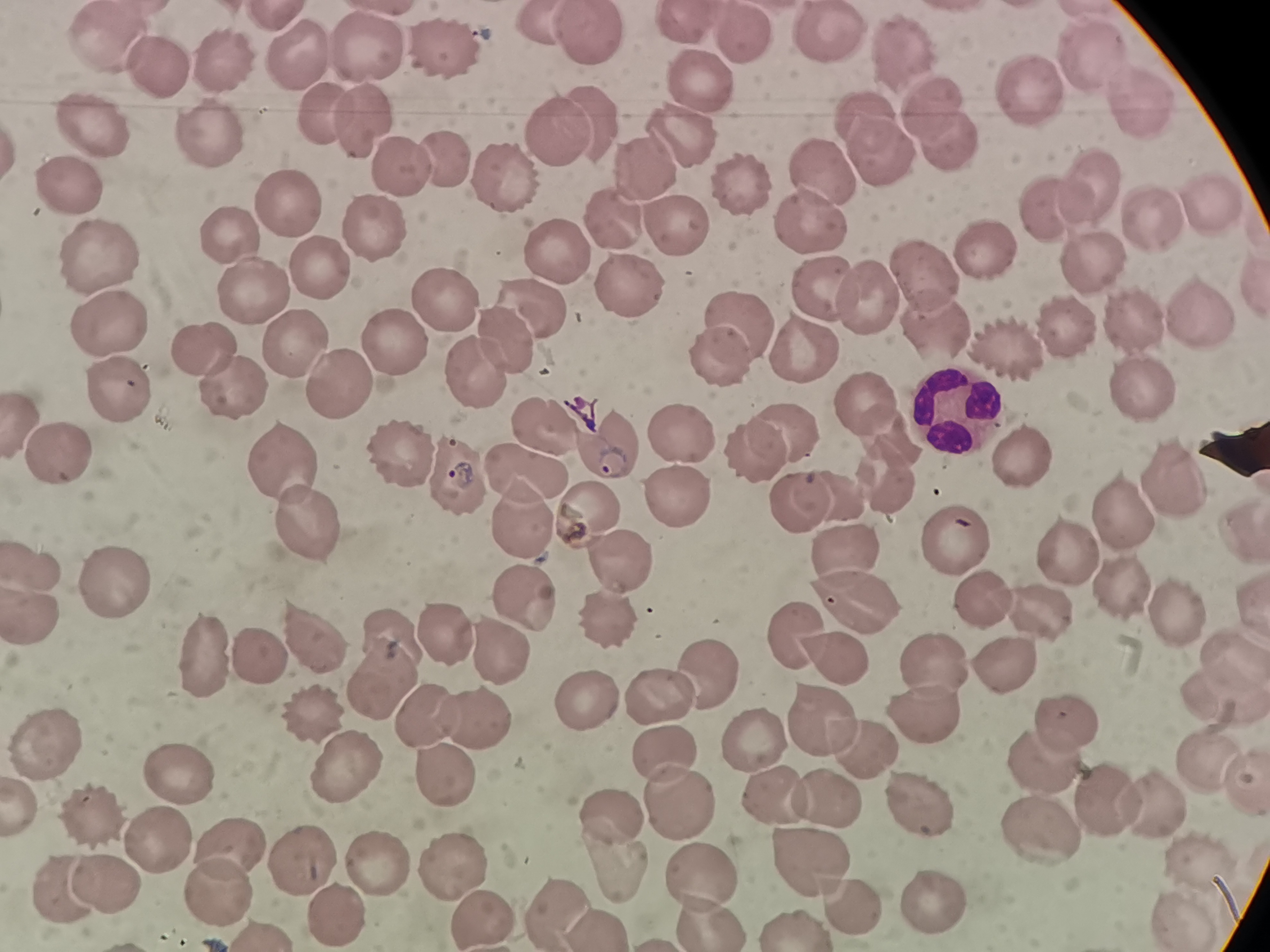
cell locations = approximate centers as [x, y] in pixels: [827, 34], [592, 36], [749, 37], [368, 44], [448, 44], [104, 47], [302, 52], [907, 55], [1093, 56], [217, 57], [164, 67], [696, 72], [1022, 86], [936, 103], [326, 105], [1137, 107], [864, 114], [369, 118], [596, 122], [90, 129], [556, 138], [690, 138], [210, 139], [948, 139], [880, 150], [439, 155], [634, 165], [399, 168], [505, 176], [825, 177], [743, 179], [1086, 185], [63, 189], [284, 201], [1214, 203], [1046, 208], [1144, 212], [813, 216], [616, 221], [679, 225], [232, 230], [365, 230], [984, 244], [559, 249], [1083, 258], [99, 259], [316, 269], [923, 270], [254, 287], [633, 289], [820, 289], [868, 293], [445, 302], [535, 302], [1197, 306], [734, 320], [937, 321], [1131, 321], [106, 322], [1071, 324], [513, 336], [388, 343], [802, 345], [1008, 345], [291, 348], [208, 349], [716, 363], [476, 374], [339, 384], [232, 386], [1140, 387], [120, 389], [863, 397], [955, 403], [782, 429], [894, 432], [676, 436], [1023, 450], [394, 453], [755, 453], [61, 454], [279, 458], [448, 470], [531, 473], [1172, 478], [887, 480], [846, 488], [676, 500], [797, 501], [599, 503], [1124, 509], [517, 515], [305, 520], [844, 539], [955, 542], [619, 557], [1071, 557], [34, 560], [109, 574], [1126, 591], [523, 599], [980, 600], [847, 603], [32, 610], [1044, 612], [606, 616], [1188, 618], [447, 627], [789, 627], [309, 636], [394, 638], [500, 648], [1227, 648], [832, 654], [204, 655], [1007, 660], [255, 661], [932, 662], [710, 670], [379, 679], [1215, 693], [657, 694], [581, 699], [310, 709], [918, 712], [819, 714], [1068, 715], [423, 716], [472, 716], [754, 735], [859, 740], [48, 742], [667, 745], [1204, 759], [1043, 760], [179, 769], [442, 770], [346, 772], [773, 786], [918, 795], [681, 796], [828, 801], [1108, 803], [1153, 804], [609, 810], [92, 815], [1041, 828], [159, 831], [231, 840], [378, 855], [450, 857], [1201, 857], [803, 859], [306, 860], [692, 873], [108, 875], [215, 886], [67, 889], [931, 897], [844, 899], [558, 906], [334, 908], [1182, 908], [481, 912], [707, 915], [594, 921], [794, 923]
stain = Giemsa
capture = smartphone camera at the microscope eyepiece
image size = 1270×952 pixels
preparation = thin smear
field of view = single